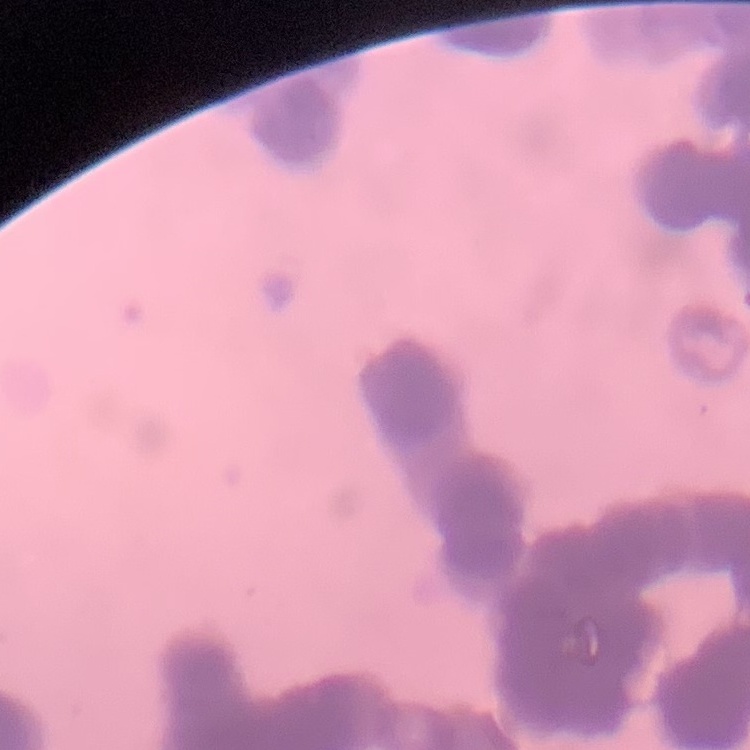 The erythrocytes exhibit rouleaux formation. Stained with either Field's or Giemsa. Thin peripheral smear. Square crop of a larger photomicrograph.